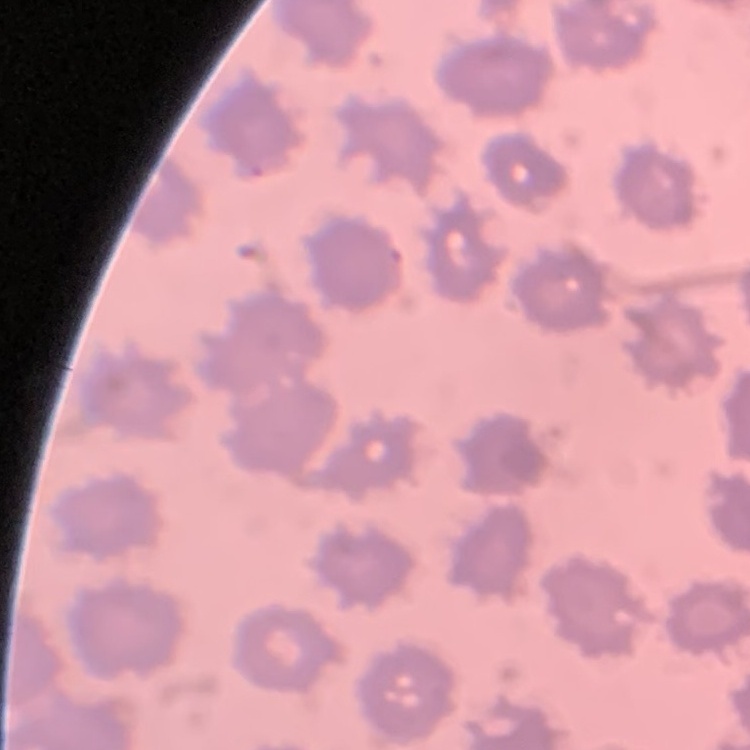 The erythrocytes exhibit no rouleaux formation. Field's or Giemsa stain. Square crop of a larger photomicrograph. Thin blood film.